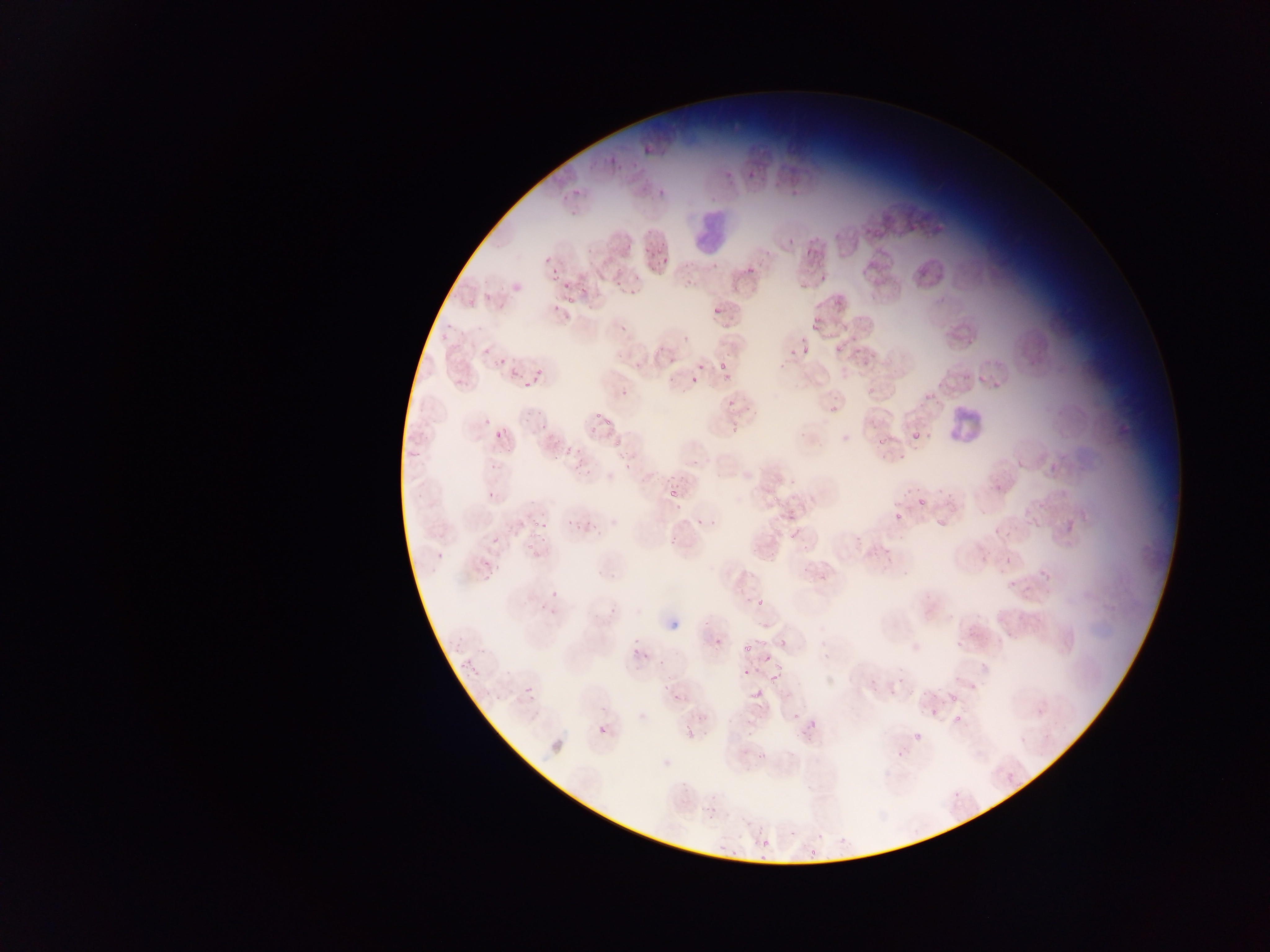

Approximate bounding boxes as left top right bottom in pixels.
Summary:
  - Plasmodium parasite locations: 547 182 582 209; 652 251 668 263; 548 270 557 280; 556 275 592 309; 709 308 721 329; 806 314 828 331; 795 338 812 359; 828 343 847 354; 718 360 731 381; 697 362 707 371; 509 367 520 378; 690 375 700 384; 827 391 854 419; 529 408 559 436; 589 408 607 431; 595 417 621 440; 721 426 741 438; 484 427 516 448; 871 432 888 450; 911 432 918 443; 622 448 642 460; 554 451 570 467; 663 489 679 504; 911 494 928 507; 890 510 904 540; 696 514 718 527; 1033 519 1043 528; 491 535 501 546; 532 537 548 546; 482 557 492 570; 1005 557 1014 565; 1008 580 1016 588; 747 595 772 614; 626 635 645 663; 739 643 758 663; 462 658 474 670; 762 666 788 684; 523 683 535 694; 751 688 762 698; 942 688 971 705; 669 697 691 711; 952 701 975 737; 926 706 940 718; 1036 707 1046 717; 593 711 617 744; 792 712 801 721; 682 729 700 749; 911 736 921 744; 1019 736 1027 744; 1006 774 1015 784; 952 791 968 802; 761 839 772 849; 808 848 818 856
  - Leukocyte locations: 686 212 759 257; 943 398 1007 453
  - Country: Ghana
  - Preparation: thin blood smear
  - Capture: mobile-phone photograph through a microscope
  - Field of view: single
  - Image size: 1270×952 pixels